Mark where platelets are.
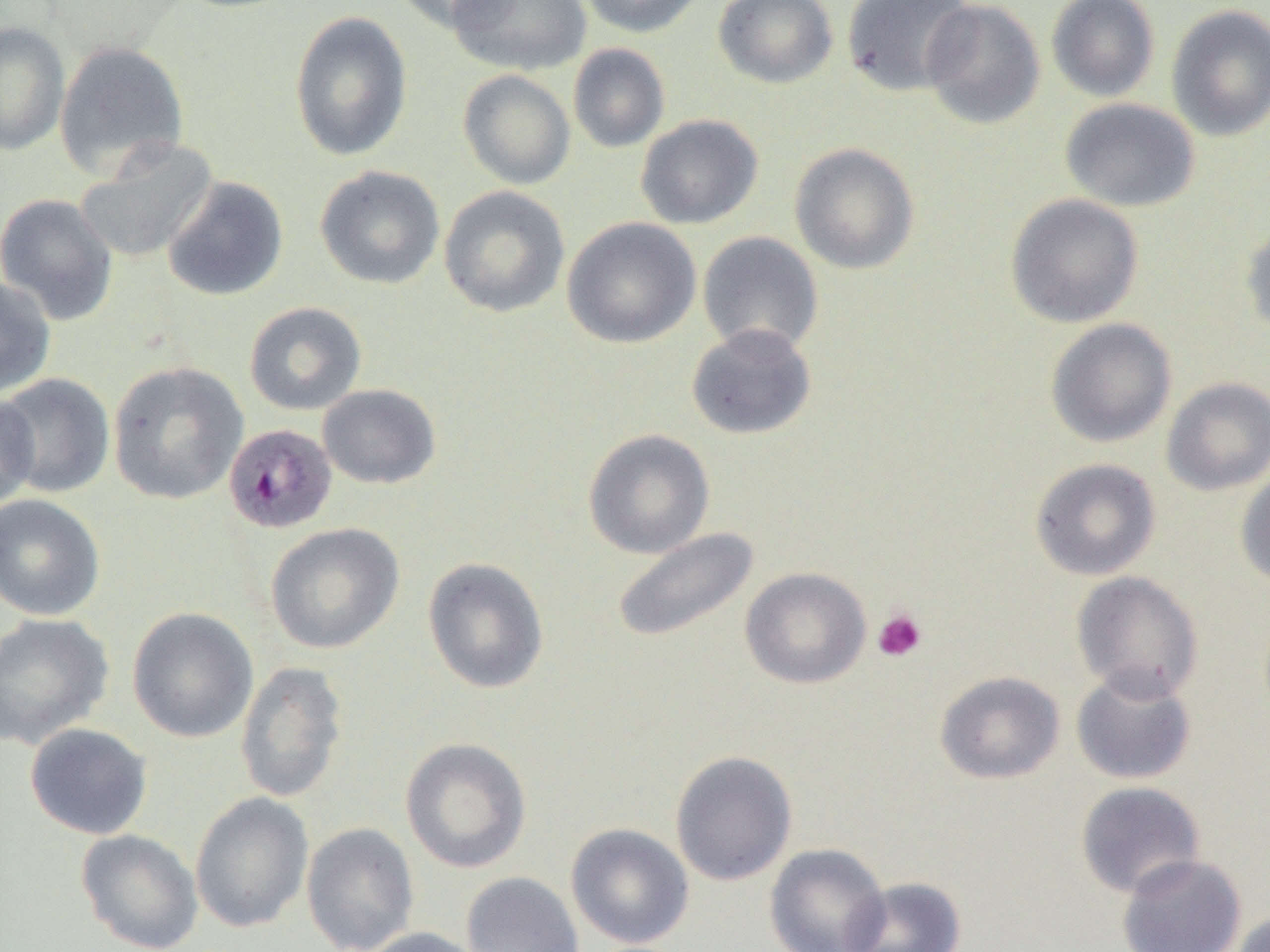
Approximate bounding boxes as [x1, y1, x2, y2] in pixels.
Platelets: [872, 608, 927, 662].

Summary:
  - Uninfected red blood cell locations: [388, 0, 519, 33], [447, 0, 591, 76], [576, 0, 707, 37], [713, 0, 838, 89], [840, 0, 975, 97], [1046, 0, 1160, 102], [920, 1, 1045, 130], [1166, 5, 1270, 141], [288, 10, 414, 161], [0, 21, 69, 155], [54, 40, 190, 179], [567, 42, 670, 154], [457, 69, 576, 190], [1060, 98, 1201, 212], [636, 114, 764, 229], [74, 137, 218, 264], [789, 142, 921, 275], [314, 165, 445, 290], [161, 176, 289, 301], [438, 185, 570, 318], [0, 192, 119, 326], [1005, 193, 1144, 328], [562, 216, 701, 349], [1240, 220, 1270, 338], [697, 231, 824, 355], [0, 276, 56, 398], [244, 302, 366, 415], [1045, 318, 1178, 448], [686, 323, 817, 440], [108, 361, 248, 504], [0, 372, 115, 498], [1161, 377, 1270, 496], [317, 384, 442, 489], [0, 392, 40, 510], [582, 428, 716, 559], [1030, 458, 1161, 581], [1235, 470, 1270, 590], [0, 493, 106, 621], [265, 522, 405, 654], [610, 526, 760, 644], [422, 557, 549, 694], [740, 567, 871, 689], [1071, 571, 1204, 702], [127, 607, 259, 743], [0, 612, 114, 750], [235, 660, 349, 804], [1070, 667, 1196, 785], [934, 670, 1065, 784], [25, 723, 153, 840], [400, 737, 532, 873], [670, 750, 798, 886], [1075, 781, 1206, 898], [190, 791, 314, 932], [300, 821, 420, 952], [566, 823, 694, 949], [75, 829, 204, 952], [765, 843, 892, 952], [1117, 853, 1246, 952], [461, 871, 585, 952], [844, 876, 966, 952], [1230, 911, 1270, 952], [359, 926, 488, 952]
  - Plasmodium malariae-infected red blood cell locations: [223, 422, 338, 534]
  - Slide-level diagnosis: Plasmodium malariae
  - Preparation: thin blood smear
  - Magnification: 1000x
  - Field of view: one of a larger specimen
  - Image size: 1270×952 pixels
  - Modality: light microscopy